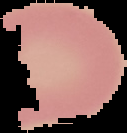
preparation = thin blood film
image type = segmented cell region with the area outside set to black
image size = 127×133 pixels
result = negative for Plasmodium parasites